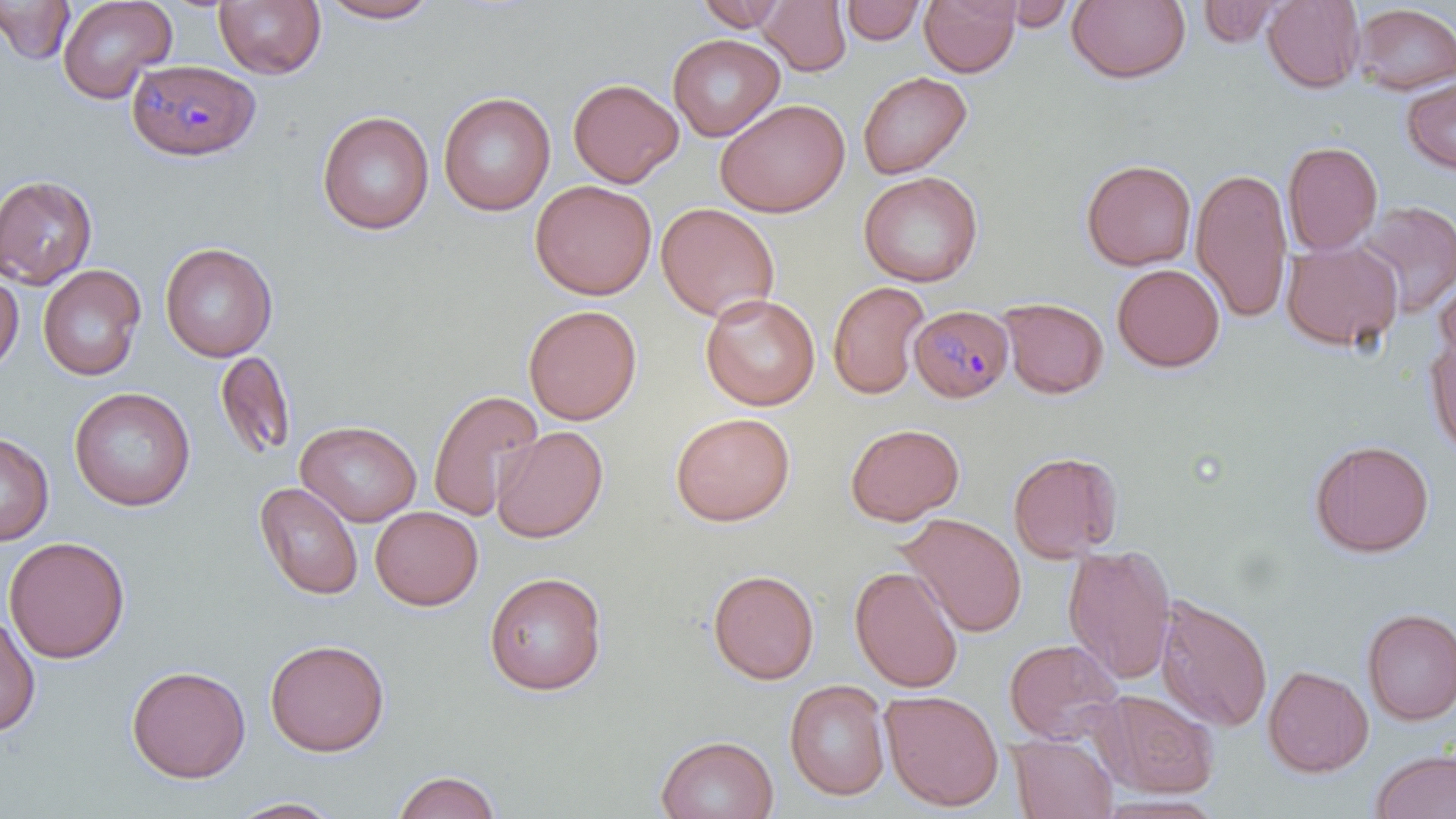 Approximate bounding boxes as (x1,y1)-(x2,y2) corner pairs in pixels. Uninfected red blood cell locations: (1,0)-(75,65), (56,0)-(177,103), (213,0)-(326,79), (316,0)-(443,24), (756,0)-(852,75), (919,0)-(1021,78), (1066,0)-(1191,85), (1262,0)-(1365,93), (695,1)-(791,32), (841,1)-(925,45), (1197,1)-(1291,47), (996,2)-(1081,30), (1352,3)-(1456,95), (667,33)-(785,141), (857,70)-(972,180), (1401,75)-(1456,174), (568,78)-(684,187), (438,91)-(555,216), (714,98)-(850,217), (316,110)-(434,235), (1283,140)-(1383,255), (1081,159)-(1197,271), (1191,166)-(1293,324), (859,171)-(983,287), (0,175)-(98,289), (530,179)-(657,300), (1356,200)-(1456,318), (655,202)-(780,322), (1281,238)-(1403,353), (159,242)-(277,361), (1112,263)-(1225,372), (38,264)-(146,381), (1435,271)-(1456,371), (0,272)-(23,375), (827,280)-(931,400), (700,293)-(820,411), (998,297)-(1109,399), (523,304)-(642,425), (1425,333)-(1456,455), (214,350)-(297,462), (69,386)-(195,511), (427,388)-(543,521), (669,412)-(795,527), (295,420)-(421,527), (845,422)-(965,525), (491,425)-(608,543), (0,431)-(54,546), (1309,439)-(1434,558), (1007,450)-(1122,563), (254,482)-(363,600), (370,506)-(483,610), (897,512)-(1027,638), (3,536)-(130,664), (1063,542)-(1176,684), (849,566)-(964,693), (707,569)-(819,685), (483,571)-(608,695), (1155,593)-(1273,732), (1360,607)-(1456,725), (0,613)-(40,738), (264,638)-(390,757), (1003,638)-(1125,746), (126,664)-(251,783), (1263,664)-(1374,777), (784,680)-(890,801), (880,689)-(1004,811), (1093,689)-(1219,798), (1008,733)-(1118,818), (655,734)-(778,819), (1370,748)-(1456,819), (392,770)-(502,818), (225,796)-(346,818). Plasmodium malariae-infected red blood cell locations: (127,59)-(260,160), (909,305)-(1014,403). Slide-level diagnosis: Plasmodium malariae. Captured at 1000x magnification. One field of a larger specimen. May-Grünwald-Giemsa-stained preparation. Image is 1456×819 pixels. Light microscopy. Thin blood film.